Assess this cell for malaria.
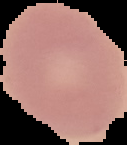

Uninfected.

Segmented cell region on a black background. Image is 127×145 pixels. From a thin blood smear.